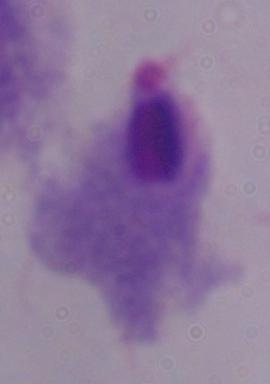 1000x magnification. A trichomonad is seen. Micrograph.